Identify the preparation type.
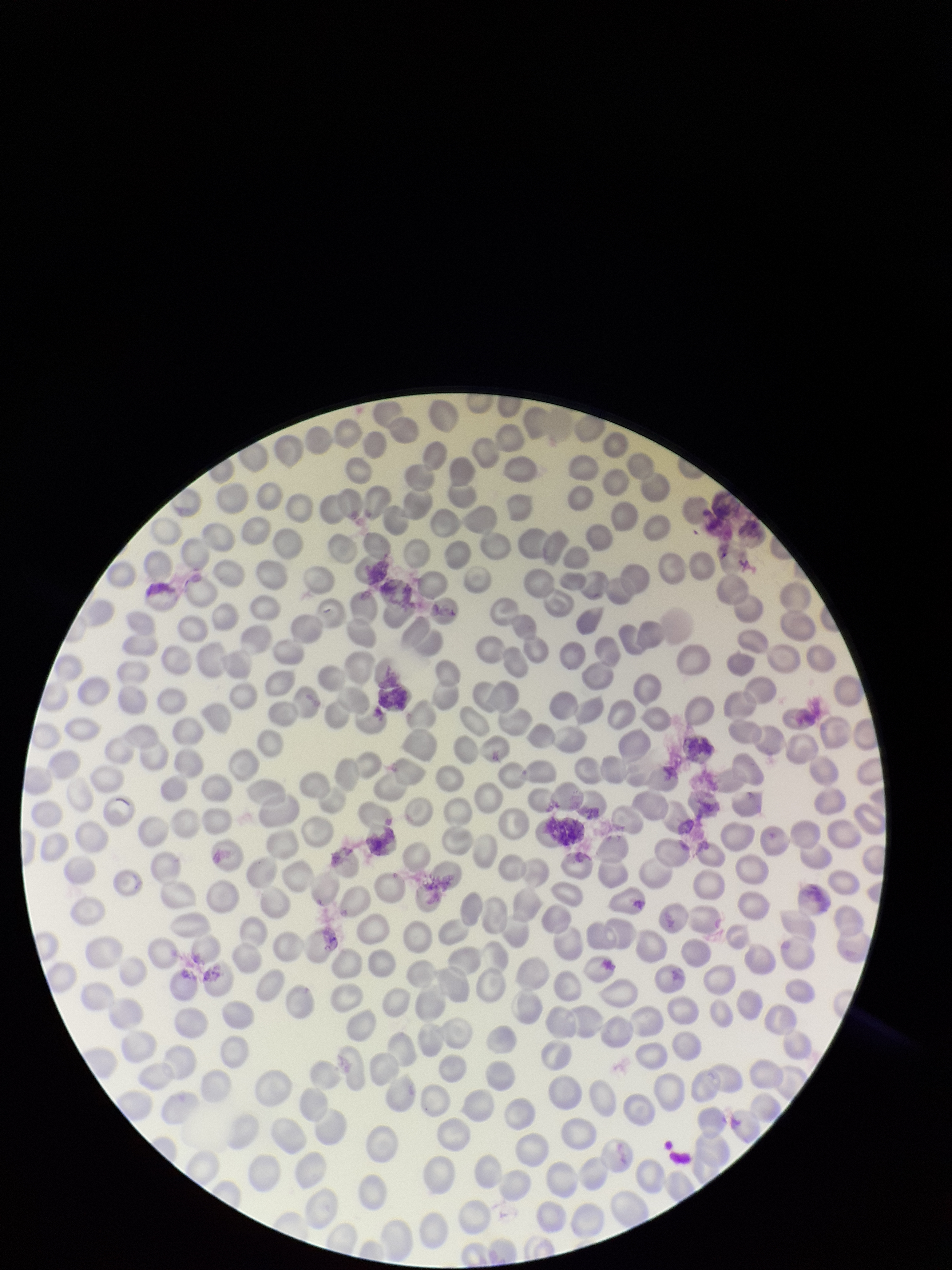

It is a thin blood smear.

Summary:
  - Image size: 952×1270 pixels
  - Parasitized red blood cells: none detected
  - Capture: smartphone photograph through the microscope eyepiece
  - Parasitized red blood cell count: 0
  - Red blood cell count: 266
  - Stain: Giemsa
  - Field of view: single
  - Patient malaria status: negative